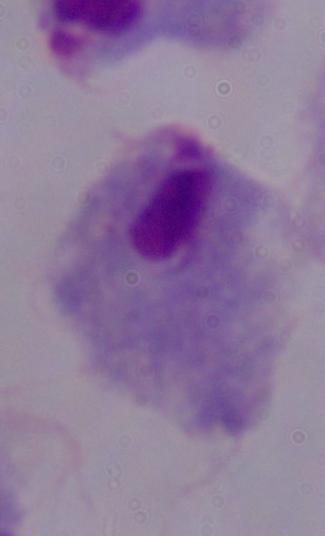

modality: micrograph
identification: trichomonad
magnification: 1000x